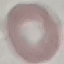

Result: no malaria parasites detected. Cell patch, automatically extracted from a larger field of view and resized to 64 × 64 pixels. Thin smear of blood. Acquired by smartphone through the microscope eyepiece. Giemsa-stained preparation.